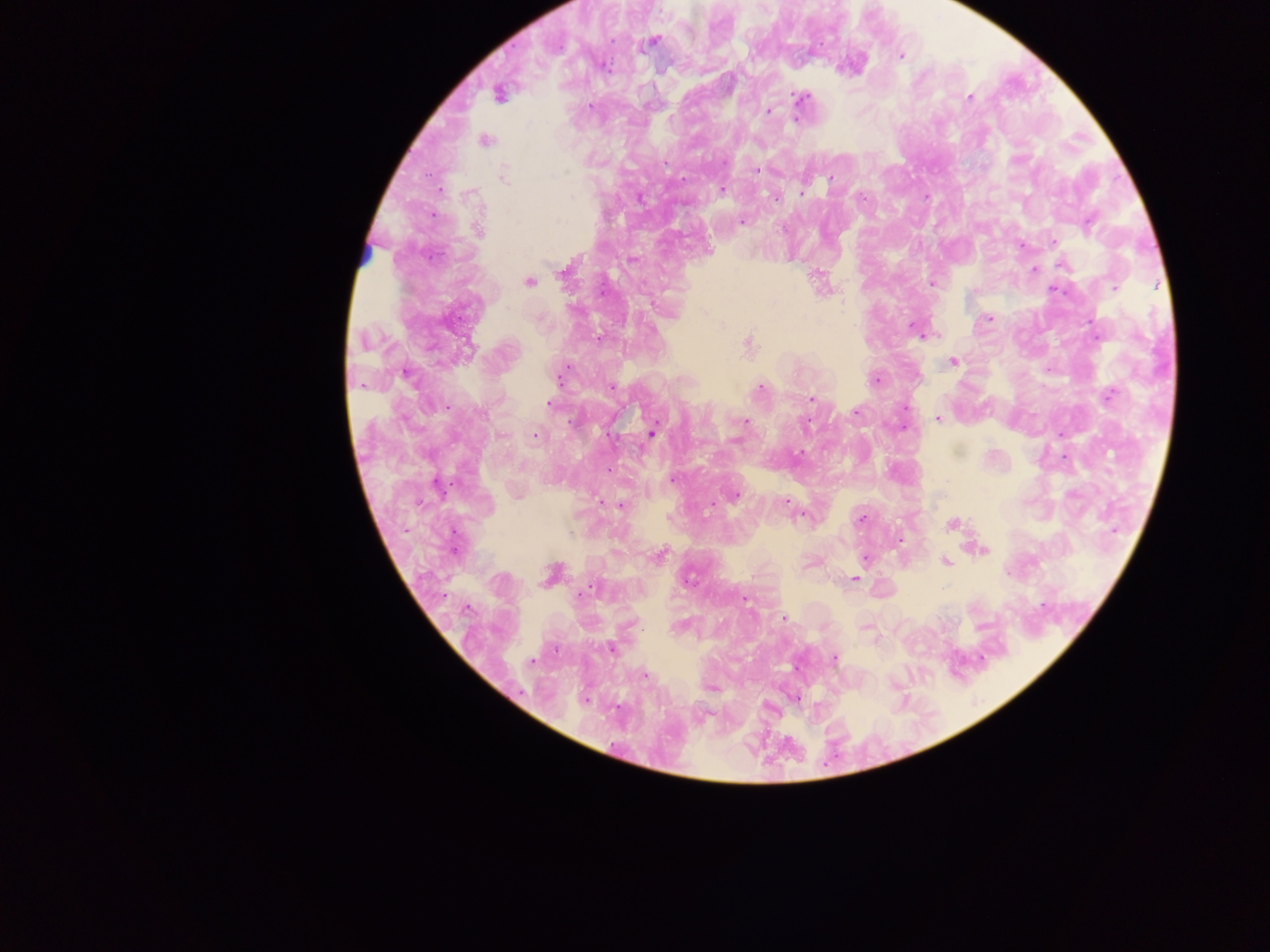 Approximate centers as {x, y} in pixels. Malaria parasite locations: {652, 41}, {901, 55}, {498, 95}, {969, 97}, {800, 98}, {590, 107}, {769, 111}, {485, 140}, {756, 170}, {504, 176}, {831, 179}, {722, 189}, {802, 191}, {926, 197}, {862, 198}, {775, 199}, {742, 222}, {479, 230}, {1054, 242}, {1022, 245}, {633, 260}, {1034, 269}, {565, 271}, {528, 282}, {932, 284}, {1114, 287}, {1054, 291}, {989, 318}, {914, 328}, {598, 339}, {748, 343}, {468, 349}, {953, 362}, {407, 375}, {559, 376}, {876, 380}, {760, 388}, {1109, 394}, {812, 398}, {549, 405}, {856, 413}, {938, 420}, {745, 421}, {806, 423}, {652, 434}, {501, 436}, {535, 436}, {672, 480}, {438, 487}, {735, 495}, {603, 501}, {786, 501}, {620, 505}, {862, 518}, {952, 525}, {984, 551}, {660, 556}, {865, 558}, {945, 562}, {854, 579}, {590, 590}, {784, 618}, {611, 649}, {834, 658}, {532, 661}, {644, 675}, {584, 698}. Photographed through a microscope with a mobile-phone camera. Image is 1270×952 pixels. Thick blood film. One field of view. Collected in Ghana.